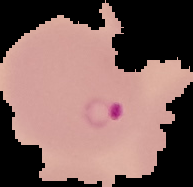 From a thin blood film. Malaria status: parasitized. The area outside the segmented cell region is set to black. Image is 193×187 pixels.